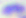 Photomicrograph. 400x magnification. Toxoplasma gondii is seen.